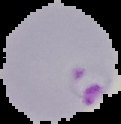
From a thin blood smear. The area outside the segmented cell region is set to black. Malaria status: parasitized. Image is 121×124 pixels.